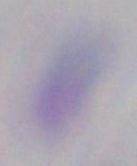

Summary:
  - Modality: micrograph
  - Magnification: 1000x
  - Identification: Toxoplasma gondii